Point out each Plasmodium parasite.
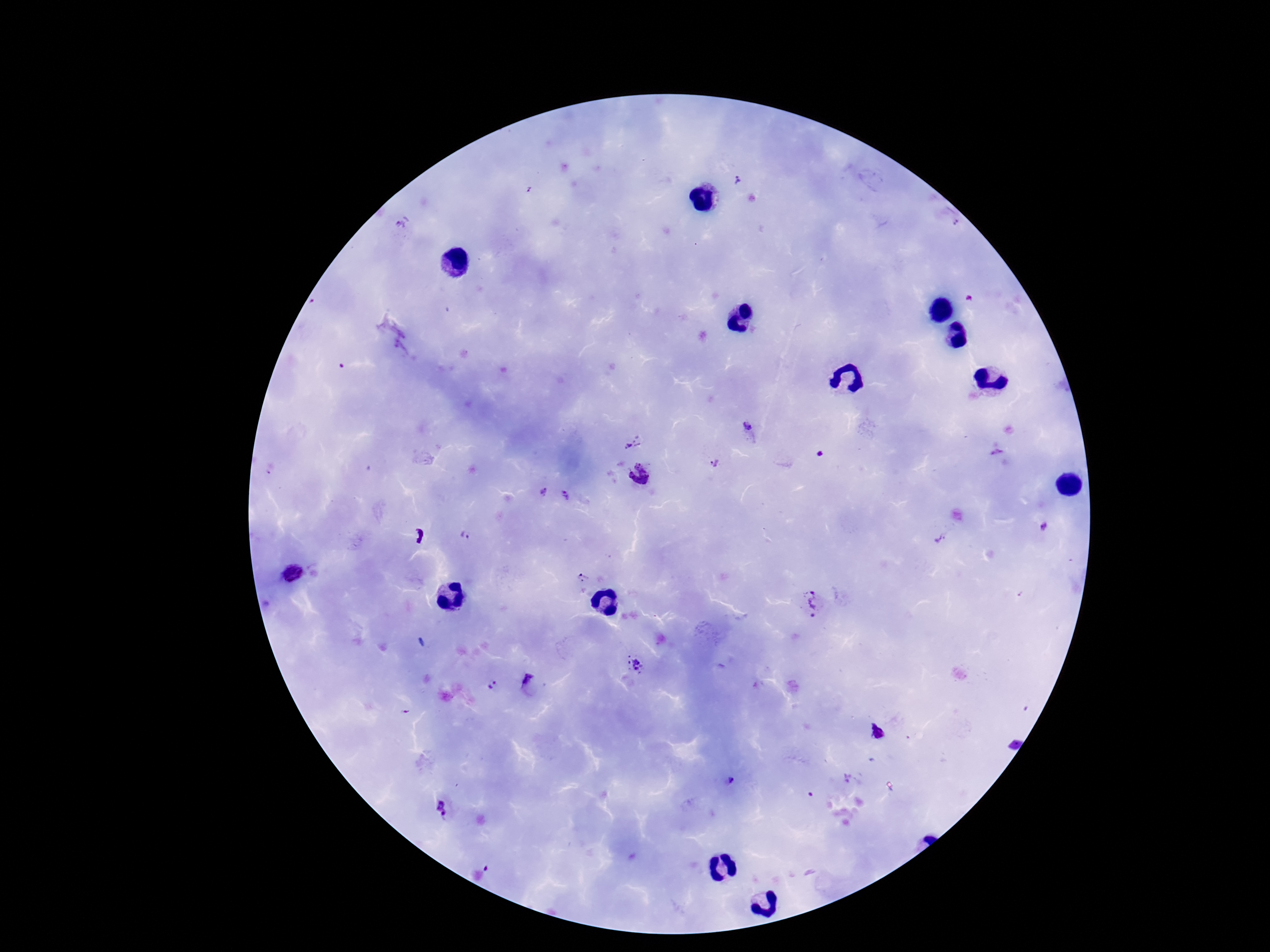

Approximate centers as [x, y] in pixels.
Plasmodium parasites: [737, 179], [749, 427], [632, 441], [819, 454], [997, 454], [713, 463], [639, 474], [539, 493], [568, 498], [1045, 527], [466, 537], [940, 538], [290, 574], [581, 577], [811, 603], [635, 665], [527, 679], [493, 686], [729, 779], [441, 810].

patient_malaria_status: positive
preparation: thick blood film
field_of_view: single
magnification: 100x
stain: Giemsa
image_size: 1270×952 pixels
capture: smartphone camera through the microscope eyepiece